Report the malaria status of this cell.
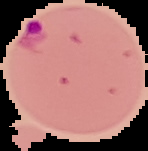

Parasitized.

Image is 148×151 pixels. From a thin blood smear. Segmented cell region on a black background.